Give the position of every Plasmodium parasite visible.
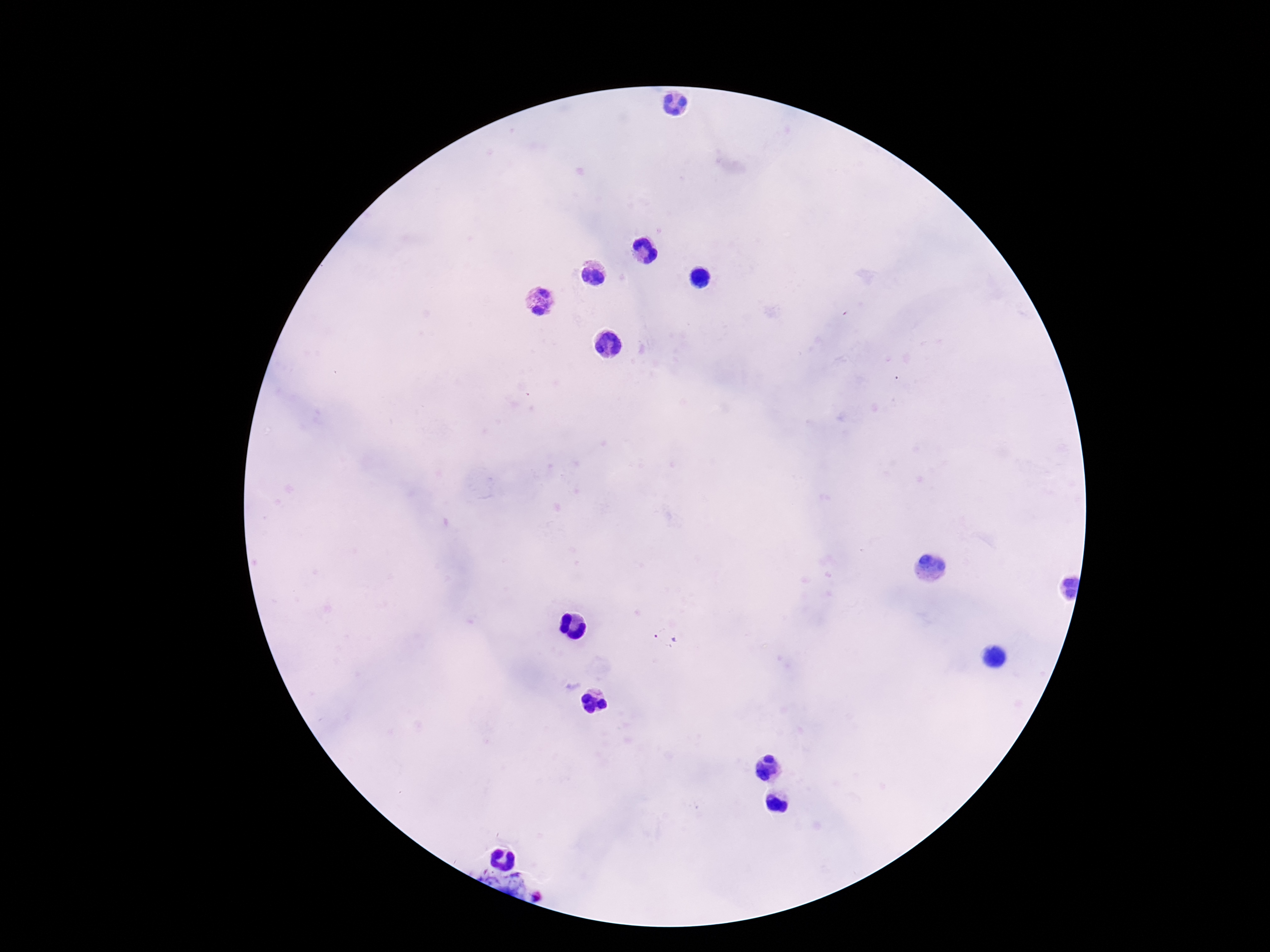
Approximate centers as {x, y} in pixels.
Plasmodium parasites: {666, 640}, {540, 898}.

Thick blood smear. Image is 1270×952 pixels. 100x magnification. Giemsa-stained preparation. Patient malaria status: positive. Smartphone photograph taken through the microscope eyepiece. Single field of view.